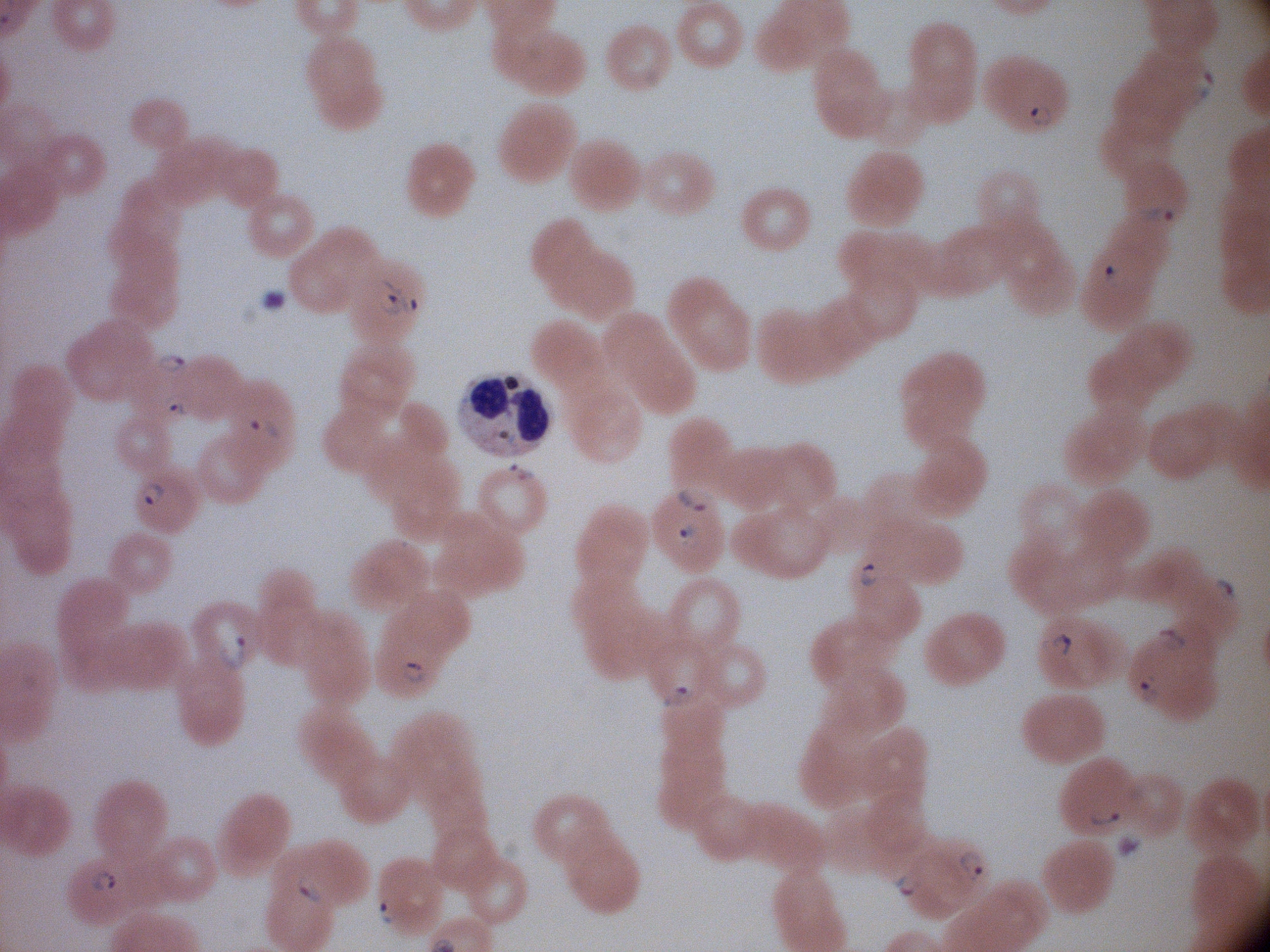

Approximate bounding boxes as named x1/y1/x2/y2 corners in pixels, from the source annotation, which is not necessarily exhaustive.
Summary:
  - Ring form locations: (x1=1192, y1=67, x2=1217, y2=104), (x1=1027, y1=103, x2=1057, y2=130), (x1=1137, y1=204, x2=1177, y2=229), (x1=1097, y1=262, x2=1127, y2=290), (x1=379, y1=276, x2=423, y2=320), (x1=154, y1=349, x2=194, y2=377), (x1=158, y1=391, x2=190, y2=420), (x1=240, y1=411, x2=280, y2=440), (x1=505, y1=459, x2=538, y2=485), (x1=138, y1=478, x2=172, y2=514), (x1=676, y1=480, x2=710, y2=517), (x1=674, y1=517, x2=707, y2=552), (x1=853, y1=558, x2=885, y2=591), (x1=1211, y1=576, x2=1241, y2=605), (x1=1156, y1=624, x2=1186, y2=652), (x1=215, y1=630, x2=252, y2=672), (x1=1034, y1=630, x2=1075, y2=660), (x1=398, y1=654, x2=435, y2=685), (x1=1135, y1=669, x2=1160, y2=708), (x1=661, y1=681, x2=695, y2=712), (x1=1087, y1=801, x2=1126, y2=830), (x1=953, y1=846, x2=992, y2=885), (x1=85, y1=863, x2=120, y2=899), (x1=891, y1=868, x2=923, y2=906), (x1=292, y1=870, x2=326, y2=904), (x1=373, y1=897, x2=402, y2=928)
  - Microscope: Leica DM2000 with built-in camera
  - Species: Plasmodium falciparum
  - Field of view: one from this slide
  - Image size: 1270×952 pixels
  - Magnification: 100x
  - Preparation: thin blood smear
  - Stain: Giemsa